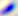
{
  "magnification": "400x",
  "modality": "micrograph",
  "identification": "Toxoplasma gondii"
}